Evaluate for Plasmodium parasites.
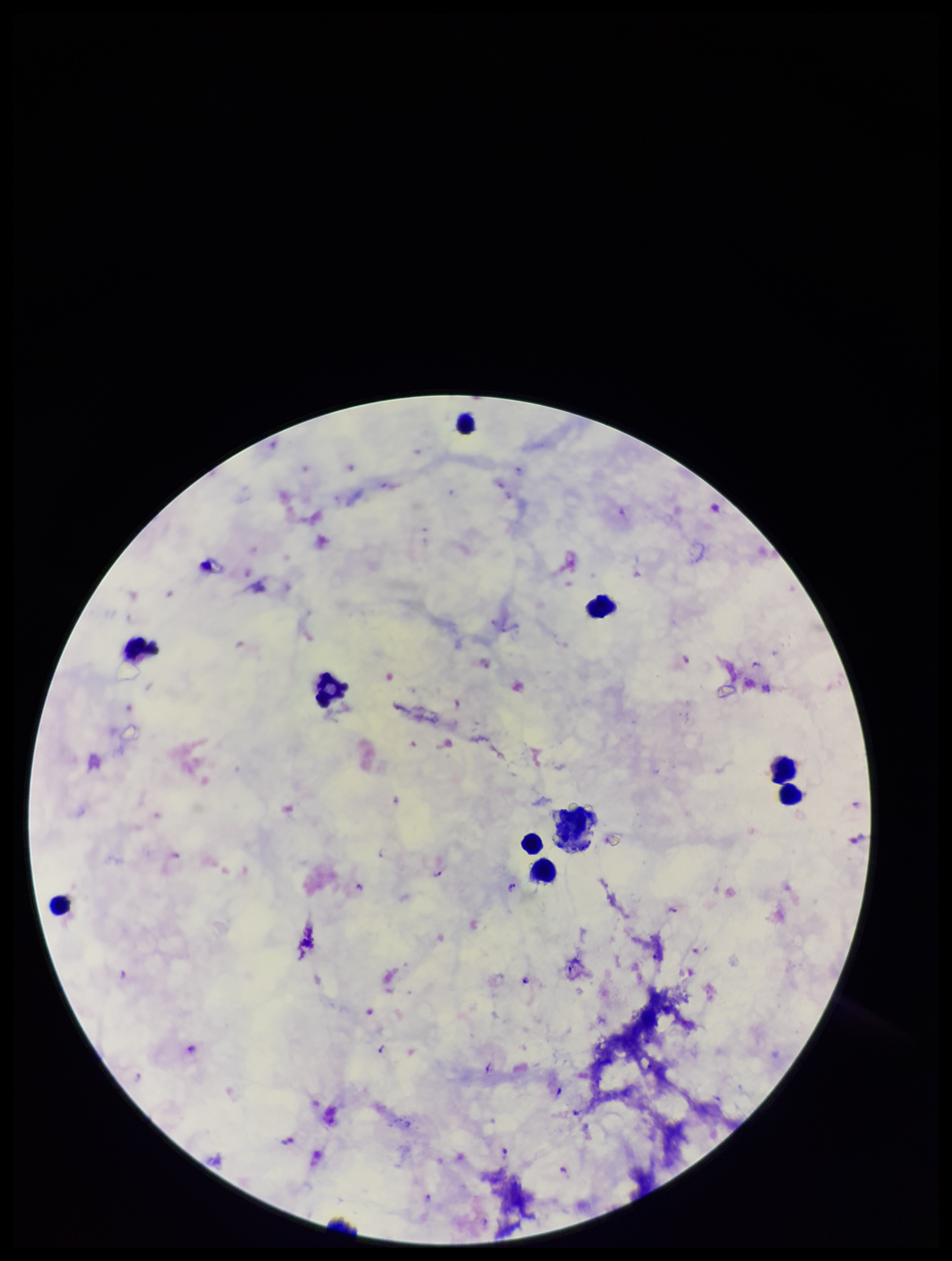
Seen.

Preparation: thick blood smear. Image is 952×1261 pixels. Species reported for this patient: Plasmodium falciparum. Giemsa stain. Parasite count: 12. Leukocyte count: 9. Single field of view. Patient malaria status: positive. Photographed through the microscope eyepiece with a smartphone camera.